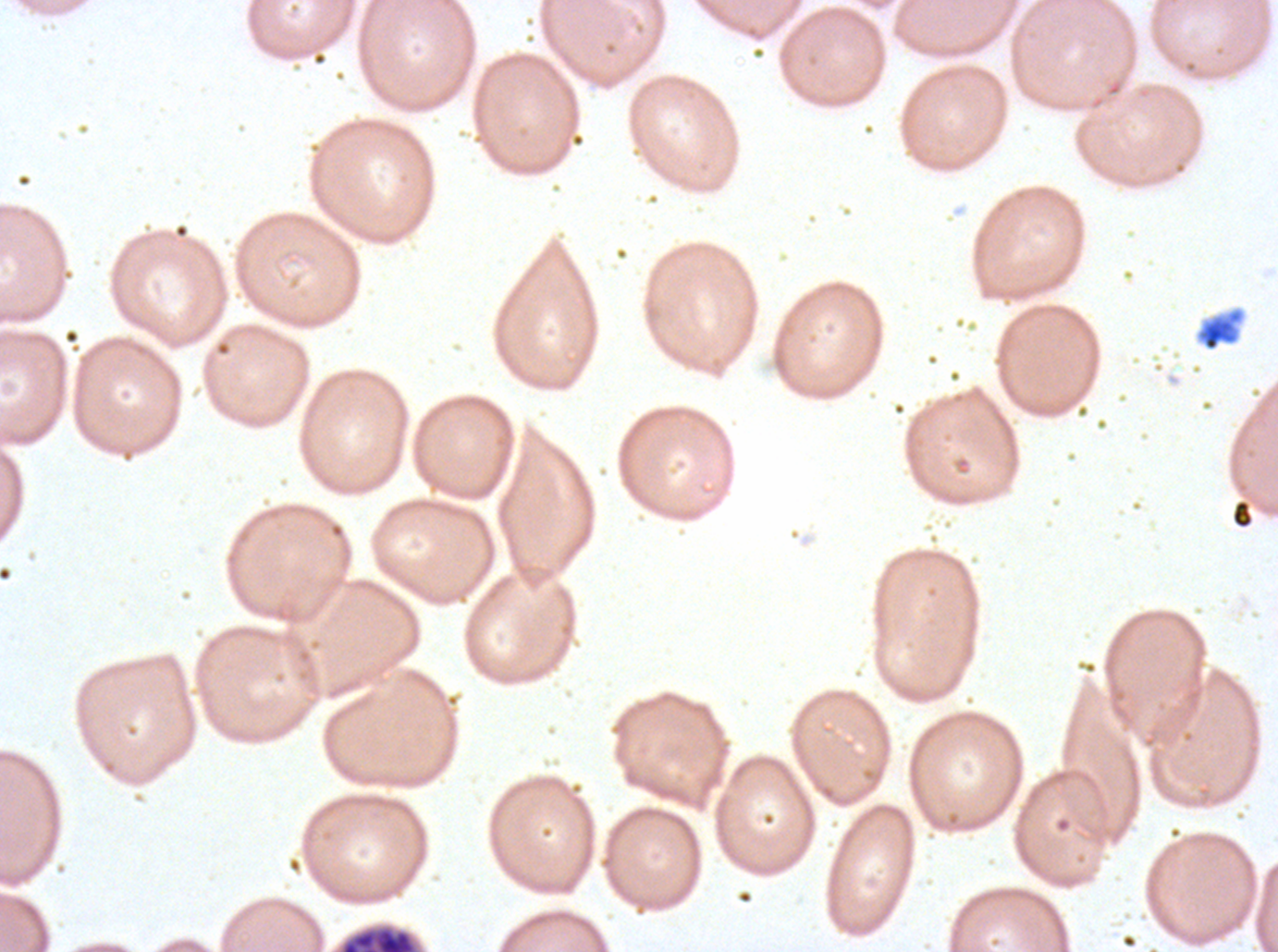
Approximate bounding boxes as (x1, y1, x2, y2) in pixels. Debris locations: (1197, 309, 1244, 352), (1231, 500, 1252, 529). Late schizont locations: (339, 925, 417, 951). Thin blood smear. Ex-vivo P. falciparum culture from a patient in The Gambia, grown for 24 to 48 hours. A sub-image separated from a larger composite. Giemsa-stained preparation. Image is 1278×952 pixels.